State the blood parasite species.
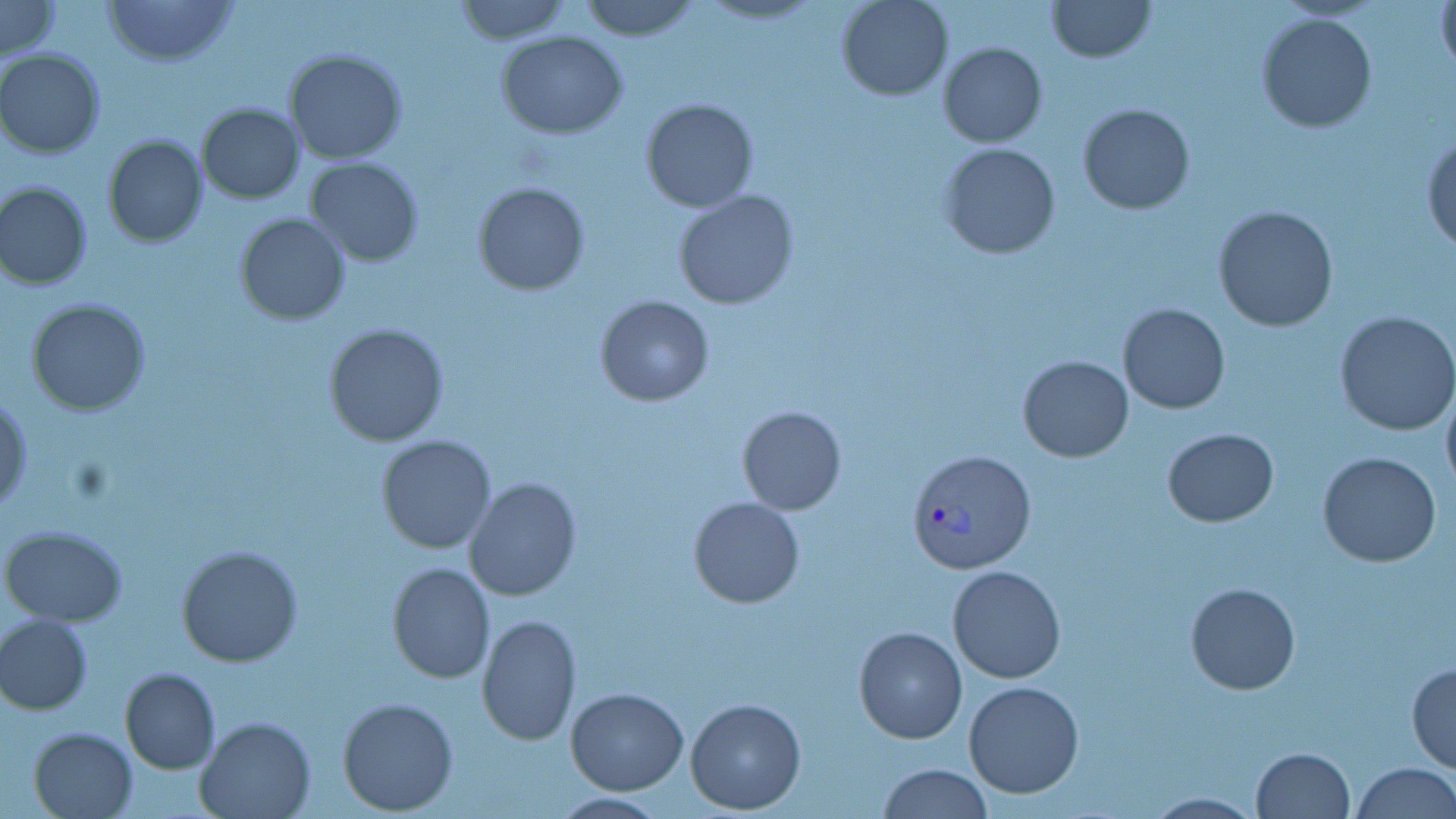
Plasmodium vivax.

Approximate bounding boxes as (x1, y1, x2, y2) in pixels. Uninfected red blood cell locations: (0, 0, 60, 59), (103, 0, 237, 67), (453, 0, 570, 43), (577, 0, 702, 43), (697, 0, 822, 26), (836, 0, 954, 101), (1043, 0, 1157, 64), (1435, 0, 1455, 81), (1256, 11, 1378, 132), (498, 30, 627, 138), (939, 41, 1048, 147), (0, 50, 105, 158), (284, 51, 409, 166), (641, 98, 760, 214), (197, 103, 304, 203), (1079, 104, 1196, 215), (1423, 130, 1456, 255), (102, 135, 208, 247), (939, 143, 1062, 260), (305, 156, 424, 267), (1, 180, 94, 290), (472, 181, 592, 296), (672, 190, 800, 311), (1212, 205, 1340, 332), (233, 212, 351, 325), (595, 295, 714, 408), (27, 297, 152, 416), (1117, 302, 1231, 415), (1334, 310, 1456, 436), (323, 322, 451, 449), (1016, 355, 1133, 462), (1441, 386, 1456, 501), (0, 396, 32, 511), (736, 406, 848, 515), (1161, 428, 1280, 527), (377, 436, 495, 555), (1317, 452, 1441, 568), (463, 477, 582, 602), (687, 497, 805, 608), (2, 524, 128, 627), (176, 543, 304, 668), (388, 563, 495, 683), (947, 564, 1066, 684), (1185, 582, 1300, 696), (475, 613, 582, 746), (0, 614, 93, 715), (854, 626, 967, 743), (1406, 662, 1456, 774), (119, 667, 220, 775), (964, 681, 1084, 800), (567, 687, 689, 796), (337, 696, 459, 816), (685, 697, 806, 815), (195, 716, 314, 819), (28, 726, 140, 819), (1250, 747, 1355, 818), (1349, 763, 1456, 819), (875, 764, 993, 819), (545, 792, 674, 819), (1138, 792, 1266, 817). Plasmodium vivax-infected red blood cell locations: (907, 449, 1036, 575). Image is 1456×819 pixels. One field of a larger specimen. Thin blood smear. 1000x magnification. May-Grünwald-Giemsa stain. Light microscopy.